Locate and identify every blood parasite.
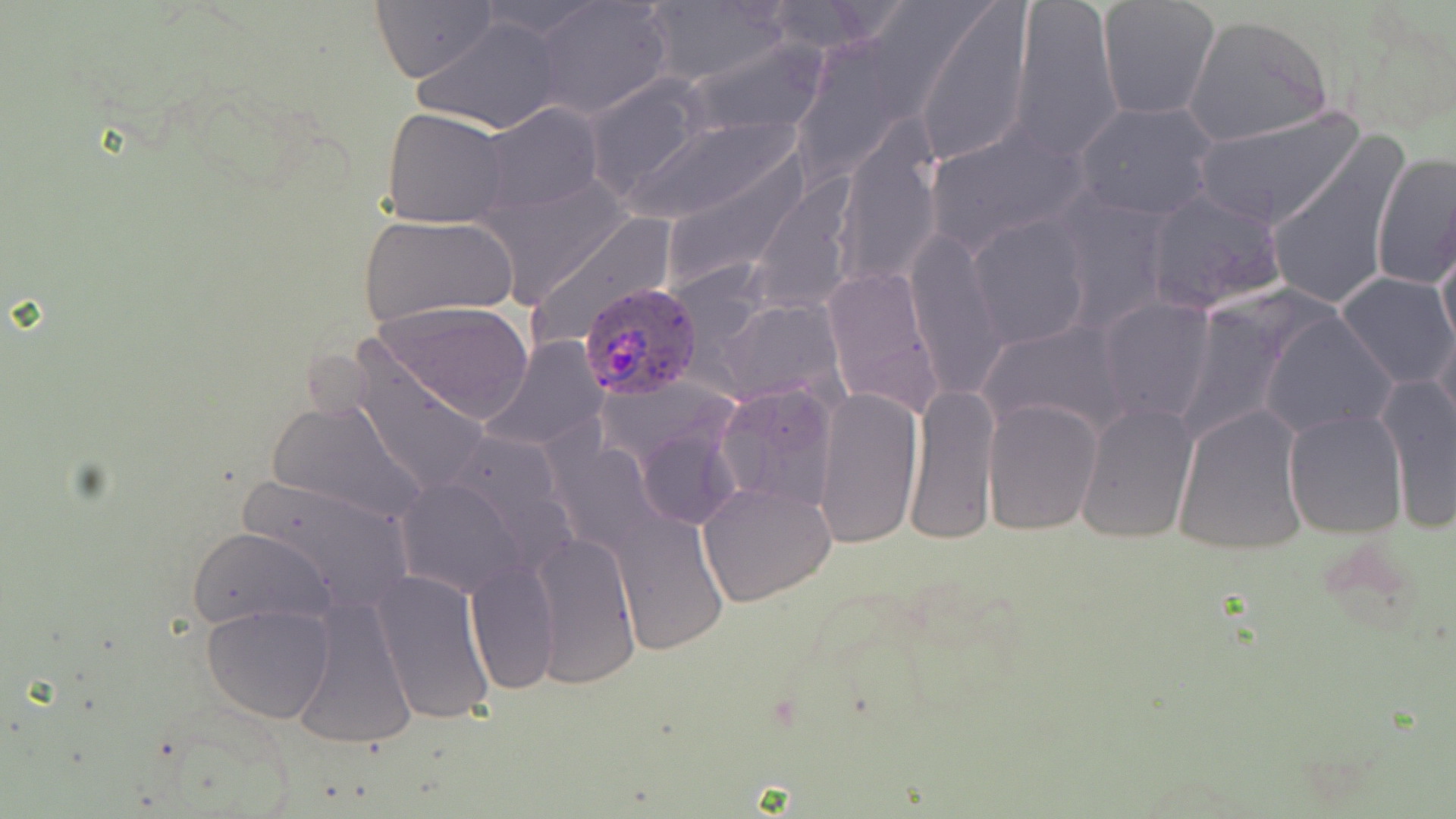

Approximate bounding boxes as (x1, y1, x2, y2) in pixels.
Plasmodium ovale-infected red blood cells: (579, 281, 704, 403).
No Plasmodium falciparum, Plasmodium malariae, Plasmodium vivax, Babesia divergens, or Trypanosoma brucei observed.

slide_level_diagnosis: Plasmodium ovale
preparation: thin blood smear
modality: light microscopy
field_of_view: one of a larger specimen
stain: May-Grünwald-Giemsa
image_size: 1456×819 pixels
uninfected_red_blood_cell_locations: 'approximate bounding boxes as (x1, y1, x2, y2) in pixels: (471, 0, 611, 39), (534, 0, 674, 120), (757, 0, 895, 56), (1010, 0, 1122, 162), (370, 1, 497, 84), (1097, 1, 1220, 121), (643, 2, 789, 90), (914, 2, 1035, 167), (1333, 7, 1456, 139), (1182, 14, 1333, 147), (413, 16, 566, 134), (681, 35, 829, 142), (583, 76, 710, 199), (1074, 101, 1220, 221), (478, 103, 603, 216), (382, 106, 511, 228), (1191, 107, 1364, 231), (614, 109, 806, 231), (925, 125, 1092, 260), (835, 126, 943, 287), (1265, 132, 1410, 315), (653, 149, 814, 296), (1370, 149, 1456, 292), (1141, 190, 1290, 318), (1052, 195, 1174, 333), (359, 213, 519, 328), (968, 214, 1093, 351), (1436, 225, 1456, 360), (905, 233, 1008, 398), (821, 266, 942, 416), (1337, 272, 1455, 390), (1098, 296, 1216, 426), (373, 299, 534, 424), (1262, 308, 1398, 439), (977, 319, 1133, 442), (483, 336, 607, 452), (346, 341, 490, 500), (1377, 373, 1456, 532), (905, 380, 1000, 546), (715, 383, 839, 514), (811, 385, 924, 550), (265, 394, 429, 528), (983, 399, 1102, 535), (1075, 401, 1198, 543), (1172, 404, 1309, 555), (1282, 408, 1407, 540), (389, 468, 539, 601), (231, 472, 417, 616), (698, 481, 837, 607), (611, 512, 727, 654), (186, 525, 336, 634), (531, 528, 642, 691), (465, 561, 559, 697), (370, 567, 497, 729), (291, 597, 417, 752), (201, 603, 335, 725)'
magnification: 1000x